Comment on the morphology of the erythrocytes.
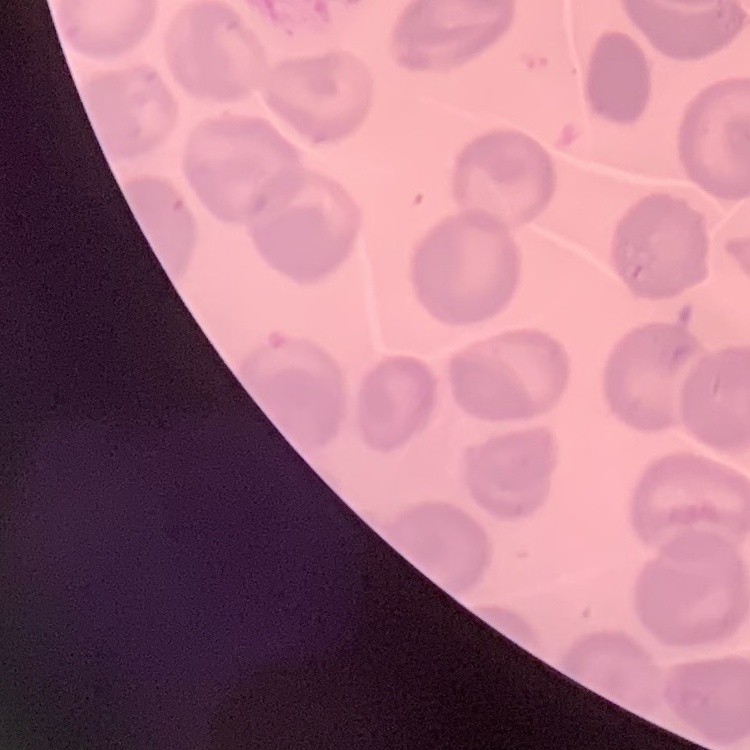

No rouleaux formation.

{
  "image_type": "square crop of a larger photomicrograph",
  "stain": "Field's or Giemsa",
  "preparation": "thin blood smear"
}